State which parasite is depicted.
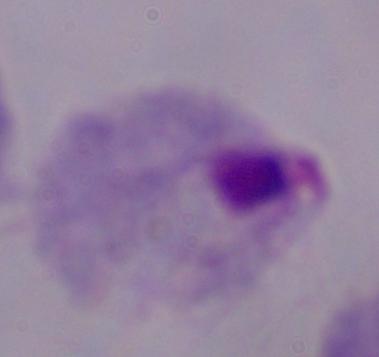
This is a trichomonad.

Micrograph. 1000x magnification.